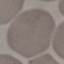

Summary:
  - Result: no malaria parasites seen
  - Capture: smartphone camera at the microscope eyepiece
  - Preparation: thin blood film
  - Stain: Giemsa
  - Image type: automatically extracted cell patch, resized to 64 × 64 pixels